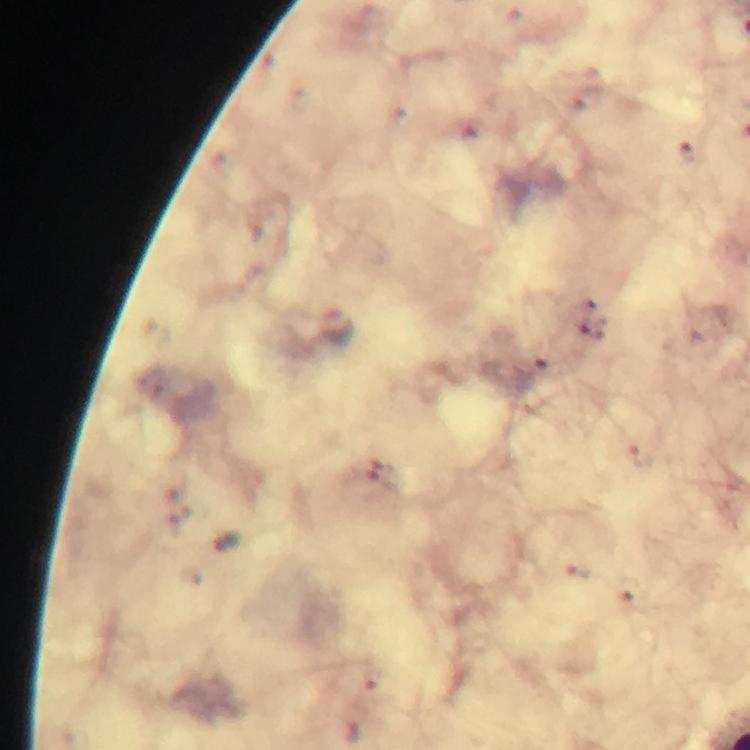
{
  "magnification": "100x",
  "preparation": "thick blood film",
  "plasmodium_parasite_locations": "approximate centers as (x, y) in pixels: (689, 152), (540, 357)",
  "capture": "smartphone photograph through a microscope",
  "context": "from a malaria diagnostic workup",
  "immersion_oil": "applied",
  "cropped_from": "one field of view",
  "image_size": "750×750 pixels",
  "stain": "Giemsa"
}